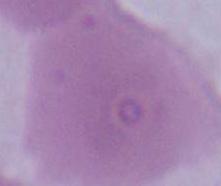

identification = red blood cell
magnification = 1000x
modality = photomicrograph